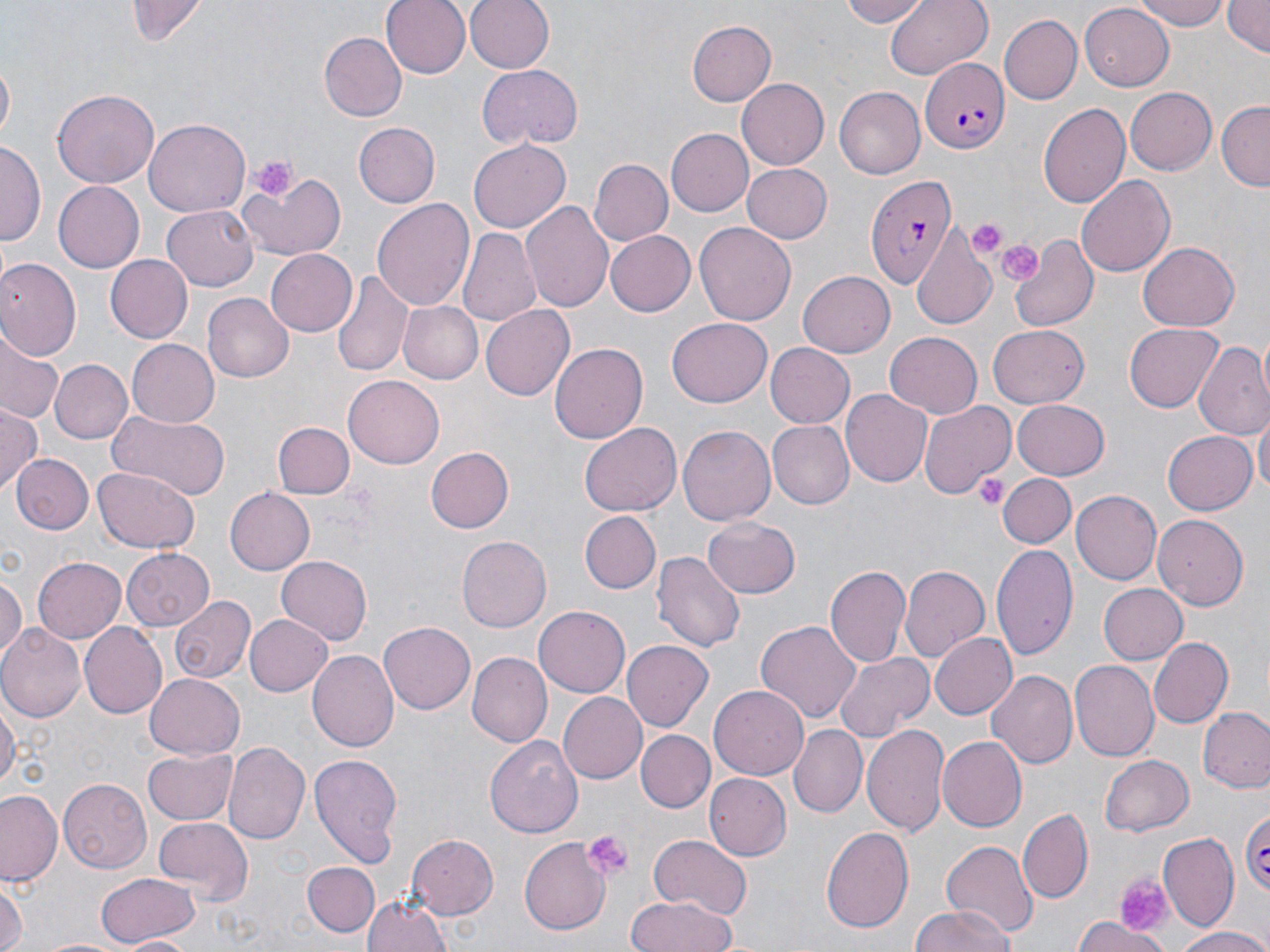

slide-level diagnosis = Plasmodium falciparum
modality = optical microscopy
magnification = 1000x
preparation = thin blood film
platelet locations = approximate bounding boxes as [x1, y1, x2, y2] in pixels: [249, 156, 296, 201], [966, 217, 1010, 257], [996, 239, 1043, 284], [971, 474, 1008, 509], [581, 828, 635, 882], [1115, 872, 1170, 935]
field of view = single
uninfected red blood cell locations = approximate bounding boxes as [x1, y1, x2, y2] in pixels: [129, 0, 206, 45], [380, 0, 469, 78], [466, 0, 555, 73], [841, 0, 929, 28], [1135, 0, 1234, 29], [1221, 0, 1269, 58], [883, 1, 991, 79], [1077, 4, 1173, 89], [998, 14, 1082, 106], [685, 18, 777, 106], [317, 33, 404, 121], [1, 62, 15, 144], [476, 66, 582, 151], [737, 78, 830, 170], [835, 87, 925, 179], [1125, 87, 1217, 175], [52, 89, 157, 189], [1216, 100, 1270, 190], [1039, 103, 1131, 209], [145, 121, 250, 217], [354, 122, 438, 207], [664, 129, 752, 217], [468, 140, 570, 233], [1, 142, 43, 247], [588, 159, 672, 246], [742, 162, 831, 242], [238, 168, 347, 260], [1077, 176, 1174, 277], [54, 182, 145, 272], [372, 198, 474, 311], [520, 200, 614, 312], [162, 205, 258, 291], [696, 221, 797, 325], [910, 223, 1001, 331], [457, 230, 541, 328], [604, 230, 694, 316], [1009, 235, 1098, 334], [1138, 243, 1240, 331], [264, 248, 357, 336], [104, 254, 194, 344], [0, 257, 82, 361], [332, 271, 415, 380], [798, 272, 896, 357], [202, 293, 293, 382], [396, 300, 482, 385], [481, 304, 575, 400], [667, 318, 771, 407], [1124, 323, 1223, 412], [987, 326, 1090, 409], [883, 332, 983, 417], [0, 334, 62, 423], [127, 339, 220, 426], [1194, 341, 1270, 442], [766, 342, 854, 429], [549, 343, 647, 446], [51, 359, 130, 443], [343, 375, 443, 467], [841, 391, 932, 488], [1012, 399, 1111, 479], [921, 400, 1016, 496], [1006, 402, 1097, 549], [0, 408, 42, 493], [106, 409, 232, 498], [1254, 414, 1268, 501], [770, 420, 855, 509], [272, 421, 353, 500], [577, 423, 680, 517], [677, 425, 775, 527], [1162, 430, 1256, 516], [424, 445, 513, 532], [12, 455, 93, 535], [93, 468, 200, 554], [999, 473, 1077, 549], [222, 486, 314, 577], [1071, 490, 1161, 585], [580, 511, 661, 593], [1152, 514, 1248, 612], [705, 516, 800, 598], [456, 536, 551, 633], [991, 541, 1077, 661], [121, 547, 213, 630], [650, 552, 744, 654], [277, 555, 371, 645], [33, 557, 127, 640], [825, 563, 910, 669], [899, 564, 991, 665], [0, 568, 25, 665], [1097, 582, 1187, 665], [170, 595, 255, 684], [533, 605, 629, 696], [245, 613, 333, 695], [756, 619, 861, 724], [379, 622, 474, 715], [78, 623, 168, 719], [0, 625, 86, 723], [930, 631, 1017, 721], [1149, 638, 1232, 727], [622, 640, 712, 732], [309, 650, 398, 750], [834, 651, 931, 741], [468, 653, 551, 746], [1071, 660, 1159, 761], [988, 669, 1081, 769], [145, 674, 245, 757], [709, 684, 809, 779], [559, 691, 649, 784], [1, 694, 18, 795], [1197, 707, 1270, 794], [863, 724, 949, 836], [790, 725, 868, 816], [635, 729, 715, 813], [484, 733, 583, 838], [938, 736, 1026, 831], [224, 742, 309, 845], [142, 747, 237, 825], [309, 752, 405, 868], [1100, 754, 1195, 836], [707, 772, 791, 862], [59, 778, 153, 871], [1, 790, 63, 885], [1018, 811, 1093, 903], [153, 817, 252, 903], [819, 825, 914, 936], [409, 835, 498, 918], [646, 835, 753, 920], [1157, 835, 1239, 934], [519, 837, 609, 936], [942, 842, 1038, 939], [302, 861, 379, 936], [97, 871, 201, 946], [0, 882, 24, 952], [362, 892, 453, 952], [625, 896, 738, 952], [909, 904, 1018, 952], [1074, 916, 1167, 952], [1170, 926, 1270, 951], [120, 934, 196, 951]
stain = May-Grünwald-Giemsa
image size = 1270×952 pixels
Plasmodium falciparum-infected red blood cell locations = approximate bounding boxes as [x1, y1, x2, y2] in pixels: [922, 57, 1007, 152], [865, 172, 956, 287], [1234, 805, 1270, 895]